Locate and identify every blood parasite.
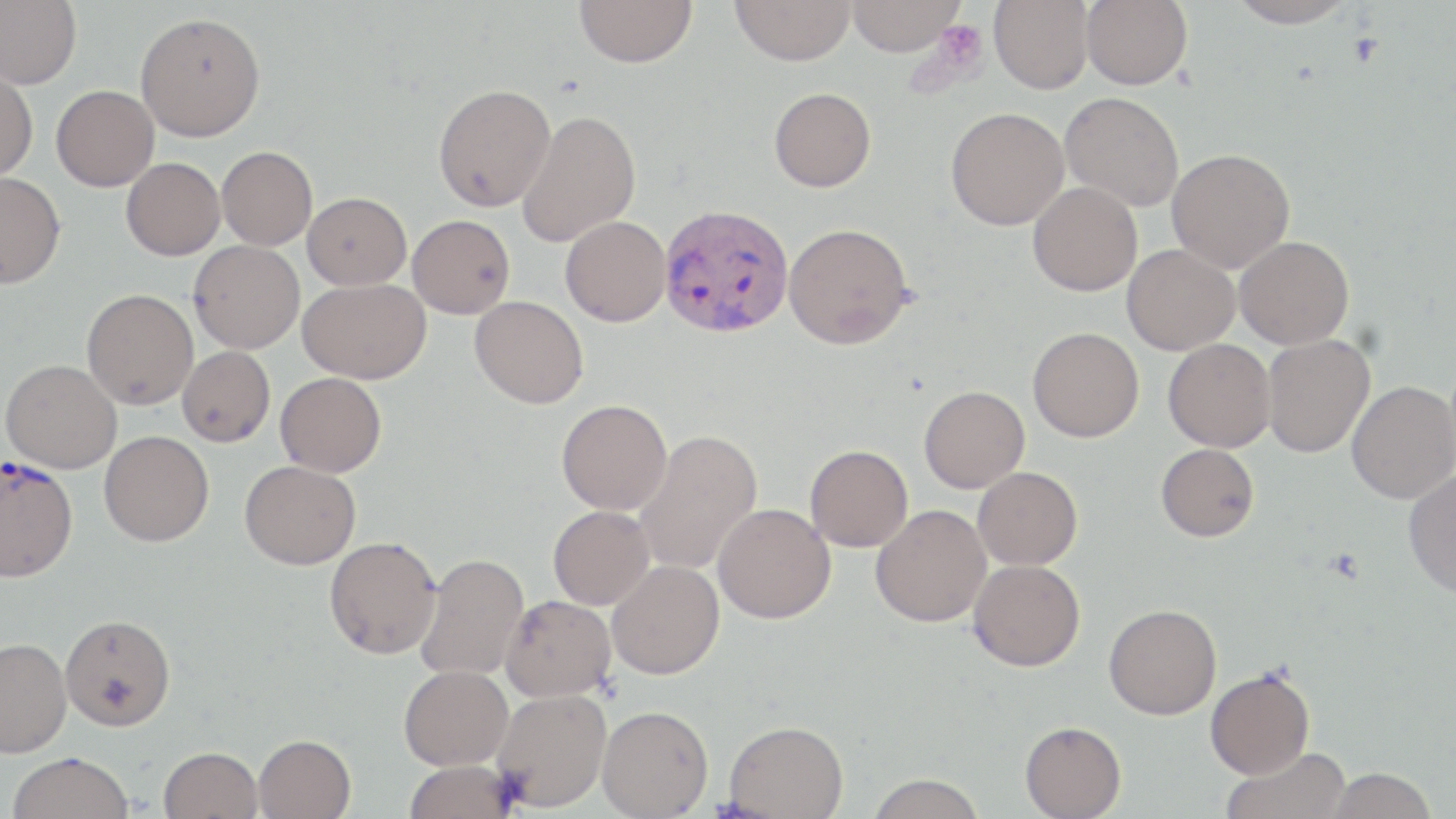

Approximate bounding boxes as [x1, y1, x2, y2] in pixels.
Plasmodium vivax-infected red blood cells: [660, 204, 793, 338], [0, 453, 78, 584].
No Plasmodium falciparum, Plasmodium ovale, Plasmodium malariae, Babesia divergens, or Trypanosoma brucei observed.

slide-level diagnosis = Plasmodium vivax
uninfected red blood cell locations = approximate bounding boxes as [x1, y1, x2, y2] in pixels: [0, 0, 81, 89], [575, 0, 697, 67], [730, 0, 856, 65], [847, 0, 965, 56], [989, 0, 1093, 94], [1081, 0, 1192, 89], [1227, 0, 1359, 28], [135, 12, 266, 142], [0, 68, 38, 181], [433, 83, 556, 211], [51, 85, 159, 191], [769, 87, 876, 192], [1059, 92, 1184, 211], [945, 107, 1069, 230], [517, 109, 641, 247], [217, 146, 318, 250], [1166, 148, 1295, 273], [121, 157, 225, 260], [0, 172, 65, 288], [1028, 182, 1142, 296], [303, 192, 411, 289], [407, 215, 515, 319], [560, 216, 671, 326], [783, 223, 912, 349], [1235, 236, 1354, 349], [189, 240, 305, 353], [1122, 244, 1239, 355], [297, 278, 430, 383], [81, 288, 198, 409], [470, 295, 588, 409], [1028, 327, 1144, 442], [1262, 334, 1374, 458], [1163, 339, 1275, 452], [177, 346, 275, 446], [1, 359, 122, 473], [275, 372, 387, 477], [1346, 381, 1456, 504], [919, 386, 1030, 493], [556, 399, 672, 515], [633, 429, 763, 576], [99, 431, 214, 546], [804, 444, 913, 552], [1155, 444, 1259, 542], [240, 460, 361, 569], [973, 467, 1082, 570], [1403, 469, 1456, 599], [712, 503, 835, 624], [871, 504, 991, 627], [548, 505, 654, 609], [324, 536, 441, 659], [416, 552, 529, 682], [968, 559, 1085, 671], [607, 560, 724, 679], [500, 595, 617, 702], [1104, 604, 1222, 719], [59, 613, 175, 730], [0, 637, 71, 757], [398, 664, 513, 770], [1205, 667, 1315, 779], [491, 688, 611, 812], [597, 705, 713, 818], [724, 720, 849, 818], [1020, 721, 1127, 819], [253, 733, 356, 819], [159, 746, 263, 819], [1222, 746, 1350, 819], [7, 752, 135, 819], [403, 758, 521, 819], [1326, 767, 1437, 818], [865, 774, 987, 818]
magnification = 1000x
preparation = thin blood film
field of view = single
image size = 1456×819 pixels
stain = May-Grünwald-Giemsa
modality = light microscopy
platelet locations = approximate bounding boxes as [x1, y1, x2, y2] in pixels: [925, 19, 989, 82]